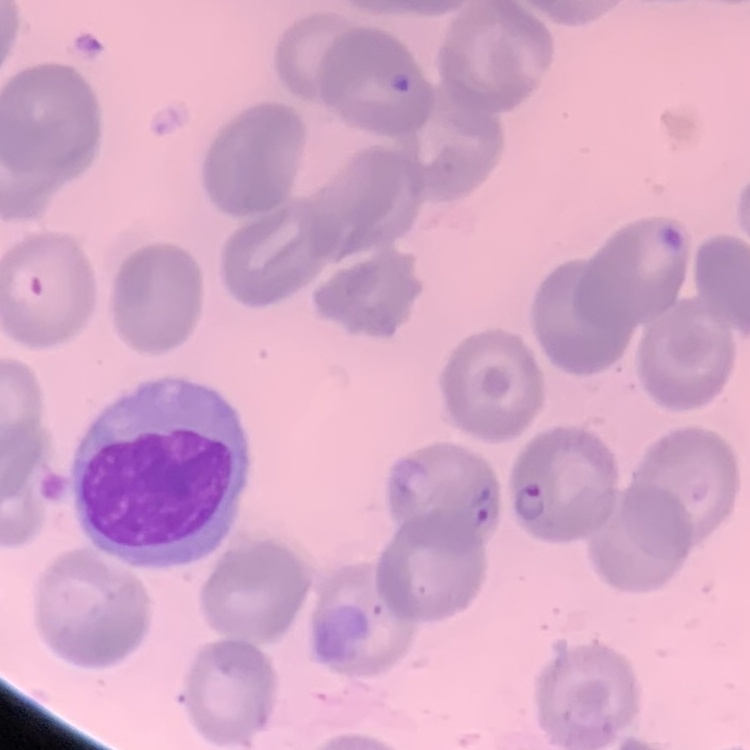
red blood cell morphology = no rouleaux formation
image type = one tile cut from a larger photomicrograph
preparation = thin blood film
stain = Field's or Giemsa